Outline each blood parasite and name the species.
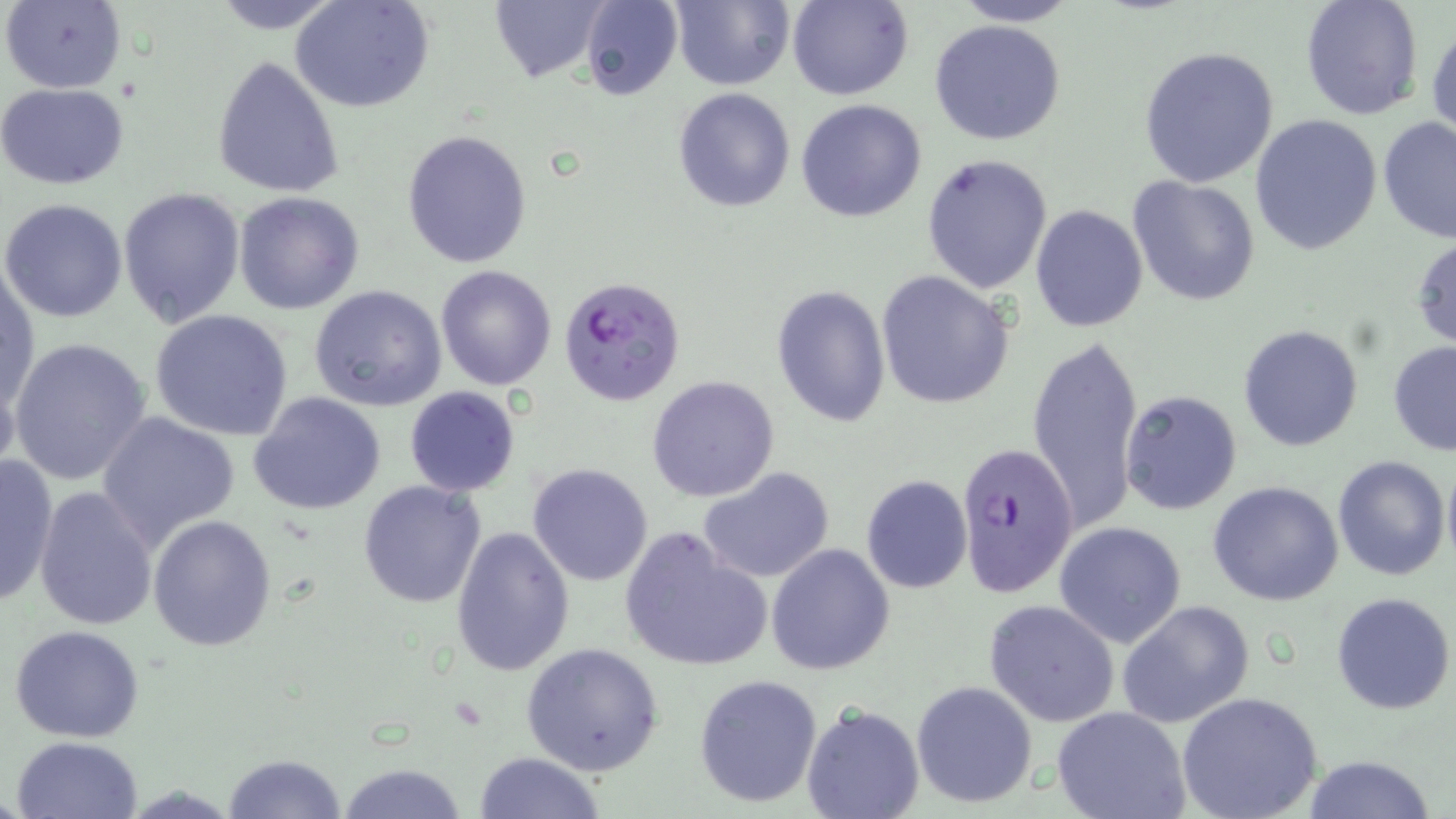
Approximate bounding boxes as [x1, y1, x2, y2] in pixels.
Plasmodium falciparum-infected red blood cells: [559, 276, 687, 406], [956, 441, 1078, 602].
No Plasmodium ovale, Plasmodium malariae, Plasmodium vivax, Babesia divergens, or Trypanosoma brucei observed.

Summary:
  - Uninfected red blood cell locations: [2, 0, 127, 94], [206, 0, 349, 32], [290, 0, 436, 114], [487, 0, 609, 84], [580, 0, 683, 100], [671, 0, 795, 90], [788, 0, 911, 101], [951, 0, 1083, 26], [1300, 0, 1426, 121], [1427, 15, 1456, 150], [929, 19, 1065, 145], [1138, 44, 1282, 187], [212, 56, 345, 199], [0, 83, 129, 188], [672, 88, 796, 211], [795, 98, 927, 222], [1250, 115, 1383, 256], [1374, 116, 1456, 244], [402, 130, 532, 268], [920, 152, 1054, 294], [1128, 175, 1261, 306], [118, 188, 246, 329], [233, 192, 365, 314], [2, 198, 128, 322], [1029, 204, 1147, 333], [1411, 233, 1456, 350], [435, 264, 558, 391], [1, 267, 39, 419], [876, 271, 1016, 410], [308, 284, 448, 411], [771, 284, 891, 427], [150, 309, 295, 441], [1238, 324, 1364, 451], [1025, 333, 1144, 532], [8, 338, 154, 487], [1388, 341, 1456, 455], [647, 374, 780, 502], [403, 386, 521, 497], [1118, 389, 1242, 515], [248, 392, 386, 516], [100, 413, 241, 548], [0, 452, 60, 607], [1333, 454, 1451, 580], [1441, 456, 1456, 575], [527, 462, 654, 586], [698, 466, 837, 583], [861, 475, 972, 593], [359, 479, 487, 608], [682, 480, 866, 644], [1208, 481, 1345, 607], [33, 486, 158, 631], [148, 514, 278, 651], [1053, 521, 1188, 648], [451, 524, 575, 676], [618, 527, 773, 673], [767, 543, 895, 674], [1332, 592, 1454, 715], [983, 598, 1120, 727], [1118, 600, 1254, 728], [9, 624, 146, 742], [522, 642, 664, 776], [693, 673, 823, 809], [911, 681, 1037, 807], [1176, 691, 1324, 819], [801, 702, 925, 819], [1051, 707, 1191, 818], [10, 735, 146, 819], [473, 752, 608, 818], [222, 753, 349, 818], [1301, 755, 1439, 819], [336, 761, 471, 819]
  - Slide-level diagnosis: Plasmodium falciparum
  - Preparation: thin blood smear
  - Modality: optical microscopy
  - Magnification: 1000x
  - Field of view: single
  - Stain: May-Grünwald-Giemsa
  - Image size: 1456×819 pixels